Describe the morphology of the red blood cells.
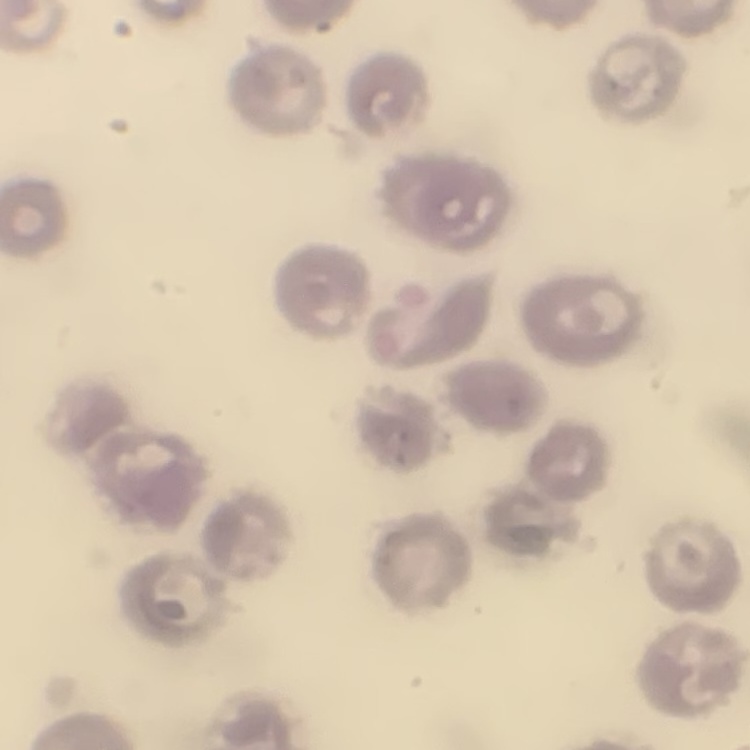
No rouleaux formation.

{
  "preparation": "thin blood film",
  "stain": "Field's or Giemsa",
  "image_type": "square crop of a larger photomicrograph"
}